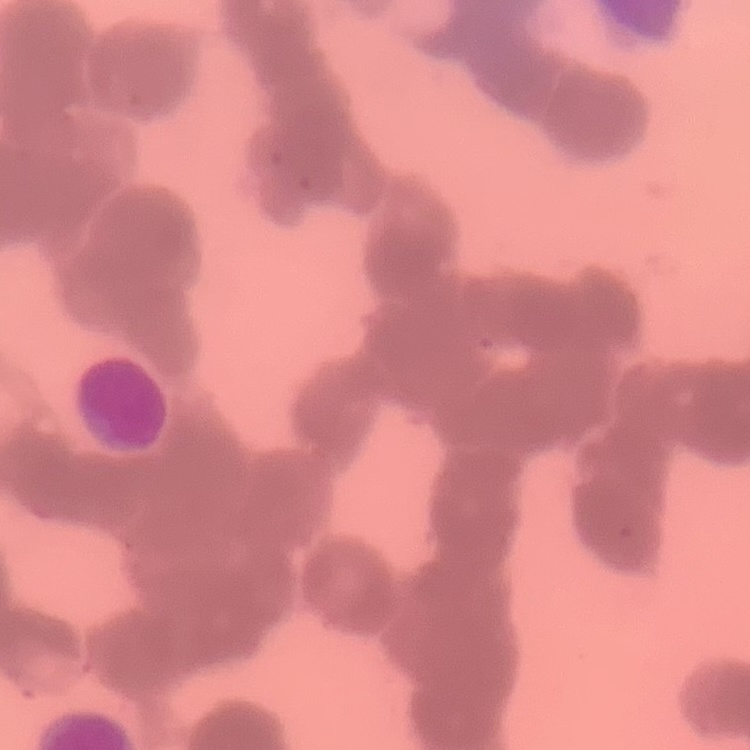
{
  "red_blood_cell_morphology": "rouleaux formation",
  "preparation": "thin blood smear",
  "image_type": "square crop of a larger photomicrograph",
  "stain": "Field's or Giemsa"
}